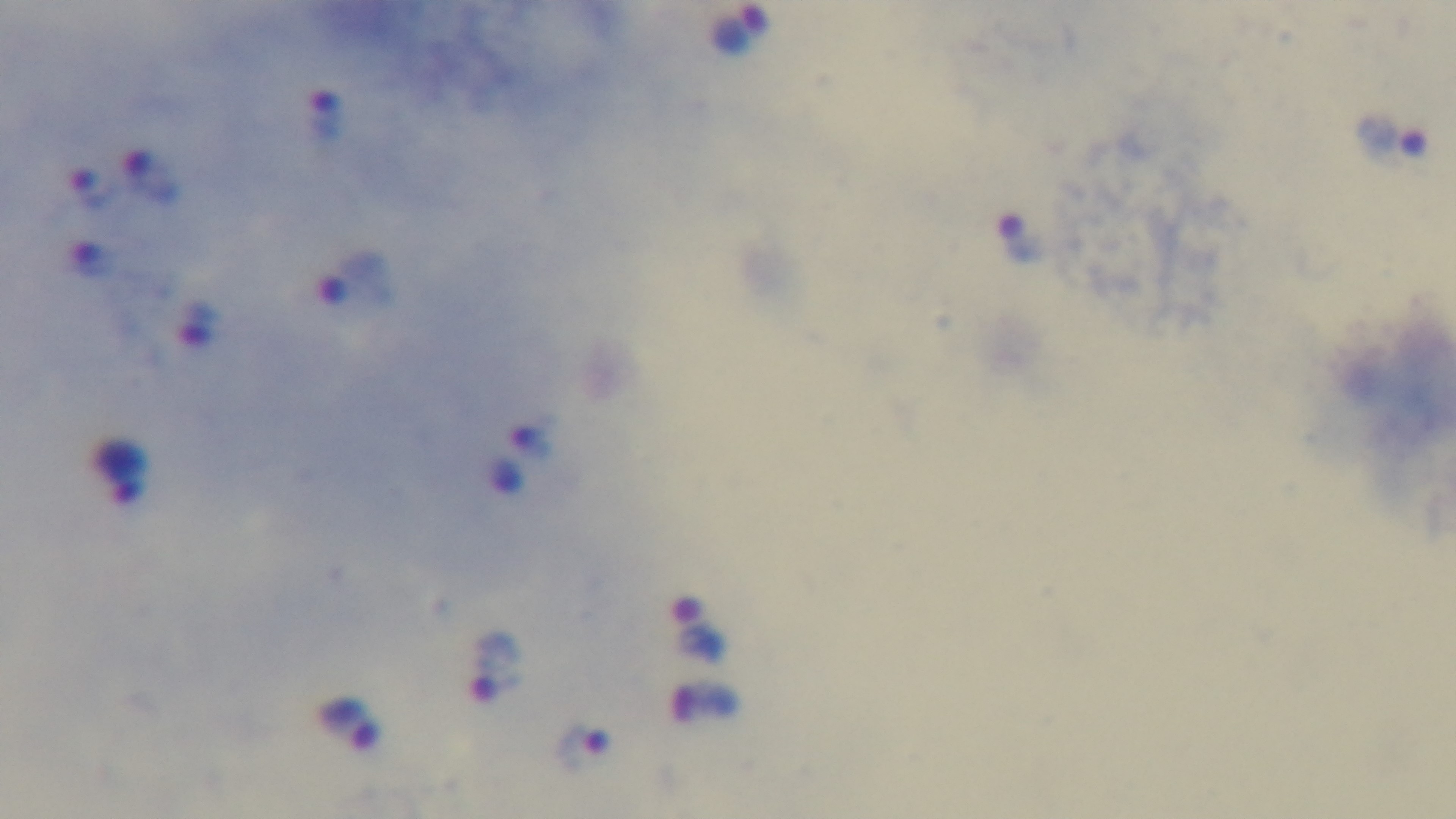

Preparation: thick. Photomicrograph. Captured with a mounted 4K digital camera. Malaria status: positive. Giemsa-stained. One field from the slide. 100x oil-immersion objective.